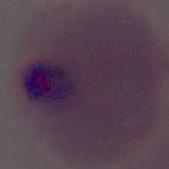
modality = photomicrograph
identification = Plasmodium
magnification = 400x or 1000x